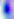
magnification = 400x
identification = Toxoplasma gondii
modality = photomicrograph